Assess this cell for malaria.
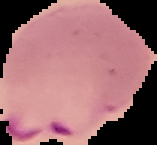

It is parasitized.

image type = segmented cell region with the area outside set to black
image size = 157×145 pixels
preparation = thin blood film